Give the preparation type.
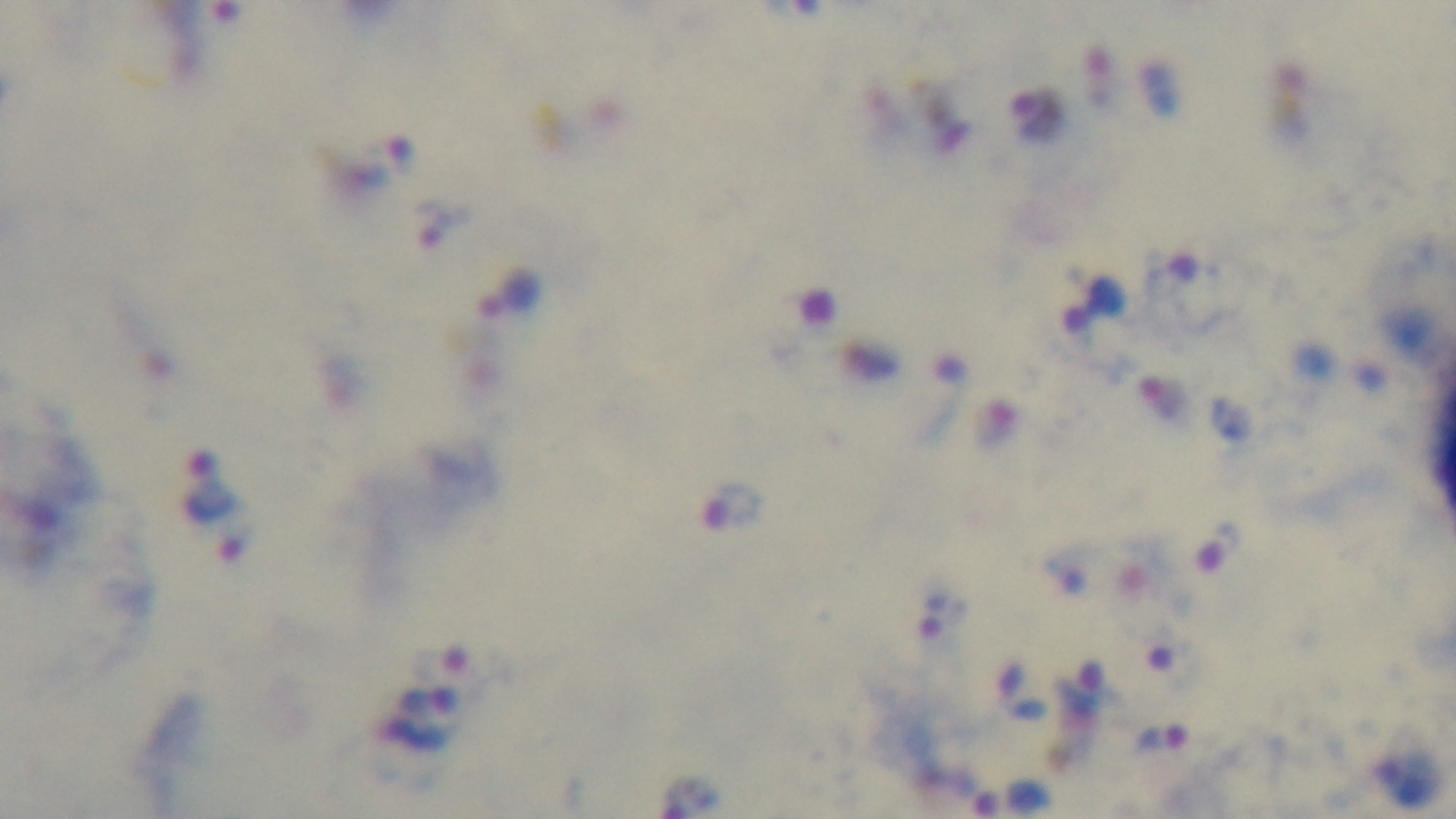
It is a thick blood film.

{
  "modality": "light microscopy",
  "capture": "mounted 4K digital camera",
  "objective": "100x oil immersion",
  "malaria_status": "infected",
  "field_of_view": "one from the slide",
  "stain": "Giemsa"
}